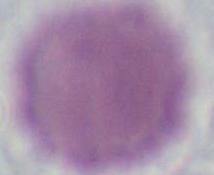

modality = micrograph
magnification = 1000x
identification = erythrocyte